Name the parasite shown.
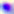

This is Toxoplasma gondii.

modality = photomicrograph
magnification = 400x